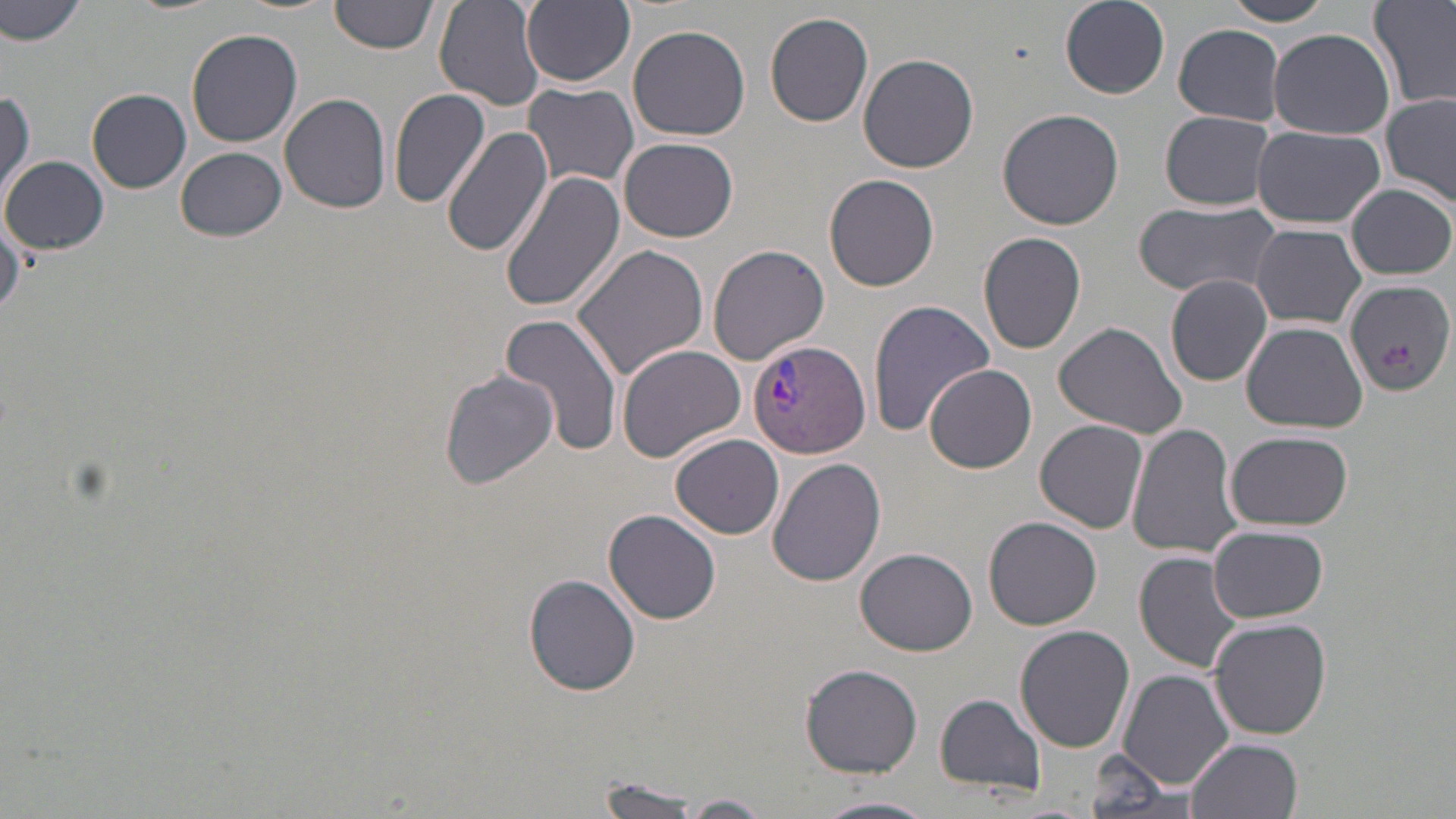
Approximate bounding boxes as named x1/y1/x2/y2 corners in pixels. Uninfected red blood cell locations: (x1=0, y1=0, x2=84, y2=50), (x1=330, y1=0, x2=437, y2=56), (x1=521, y1=0, x2=636, y2=87), (x1=1060, y1=0, x2=1173, y2=100), (x1=1219, y1=0, x2=1337, y2=27), (x1=1371, y1=0, x2=1456, y2=111), (x1=434, y1=2, x2=546, y2=111), (x1=765, y1=11, x2=874, y2=128), (x1=627, y1=24, x2=751, y2=141), (x1=1173, y1=24, x2=1286, y2=125), (x1=186, y1=28, x2=304, y2=148), (x1=1268, y1=28, x2=1394, y2=139), (x1=858, y1=52, x2=980, y2=172), (x1=523, y1=80, x2=639, y2=191), (x1=87, y1=89, x2=191, y2=193), (x1=389, y1=89, x2=492, y2=209), (x1=0, y1=92, x2=34, y2=201), (x1=279, y1=92, x2=393, y2=213), (x1=1381, y1=93, x2=1456, y2=208), (x1=998, y1=107, x2=1126, y2=230), (x1=1159, y1=111, x2=1278, y2=210), (x1=442, y1=125, x2=553, y2=257), (x1=1252, y1=126, x2=1388, y2=230), (x1=618, y1=137, x2=738, y2=242), (x1=174, y1=146, x2=287, y2=241), (x1=3, y1=154, x2=107, y2=255), (x1=501, y1=170, x2=625, y2=313), (x1=823, y1=174, x2=940, y2=293), (x1=1347, y1=184, x2=1454, y2=279), (x1=1134, y1=200, x2=1286, y2=300), (x1=0, y1=217, x2=25, y2=319), (x1=1251, y1=223, x2=1367, y2=329), (x1=978, y1=232, x2=1087, y2=355), (x1=706, y1=243, x2=830, y2=365), (x1=572, y1=244, x2=710, y2=379), (x1=1165, y1=275, x2=1273, y2=386), (x1=1345, y1=280, x2=1454, y2=396), (x1=868, y1=299, x2=994, y2=435), (x1=499, y1=314, x2=625, y2=457), (x1=1241, y1=320, x2=1367, y2=433), (x1=1053, y1=321, x2=1188, y2=439), (x1=617, y1=344, x2=746, y2=461), (x1=924, y1=364, x2=1037, y2=473), (x1=439, y1=369, x2=559, y2=492), (x1=1035, y1=419, x2=1149, y2=534), (x1=1128, y1=425, x2=1242, y2=559), (x1=1224, y1=431, x2=1353, y2=531), (x1=670, y1=434, x2=784, y2=539), (x1=769, y1=458, x2=886, y2=589), (x1=603, y1=509, x2=720, y2=623), (x1=985, y1=516, x2=1103, y2=631), (x1=1207, y1=527, x2=1328, y2=624), (x1=855, y1=547, x2=977, y2=655), (x1=1135, y1=553, x2=1245, y2=676), (x1=523, y1=574, x2=642, y2=695), (x1=1208, y1=616, x2=1333, y2=739), (x1=1017, y1=626, x2=1135, y2=754), (x1=800, y1=664, x2=923, y2=777), (x1=1120, y1=668, x2=1235, y2=788), (x1=934, y1=692, x2=1046, y2=798), (x1=1189, y1=737, x2=1306, y2=819), (x1=1086, y1=750, x2=1191, y2=816), (x1=587, y1=782, x2=713, y2=818), (x1=676, y1=794, x2=773, y2=817), (x1=820, y1=795, x2=936, y2=819). Plasmodium vivax-infected red blood cell locations: (x1=746, y1=338, x2=872, y2=460). Slide-level diagnosis: Plasmodium vivax. Light microscopy. One field of a larger specimen. Thin blood film. May-Grünwald-Giemsa stain. Image is 1456×819 pixels. Captured at 1000x magnification.